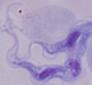

Summary:
  - Identification: trypanosome
  - Modality: photomicrograph
  - Magnification: 1000x